Name the parasite shown.
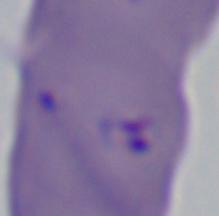

Babesia.

modality: micrograph
magnification: 1000x